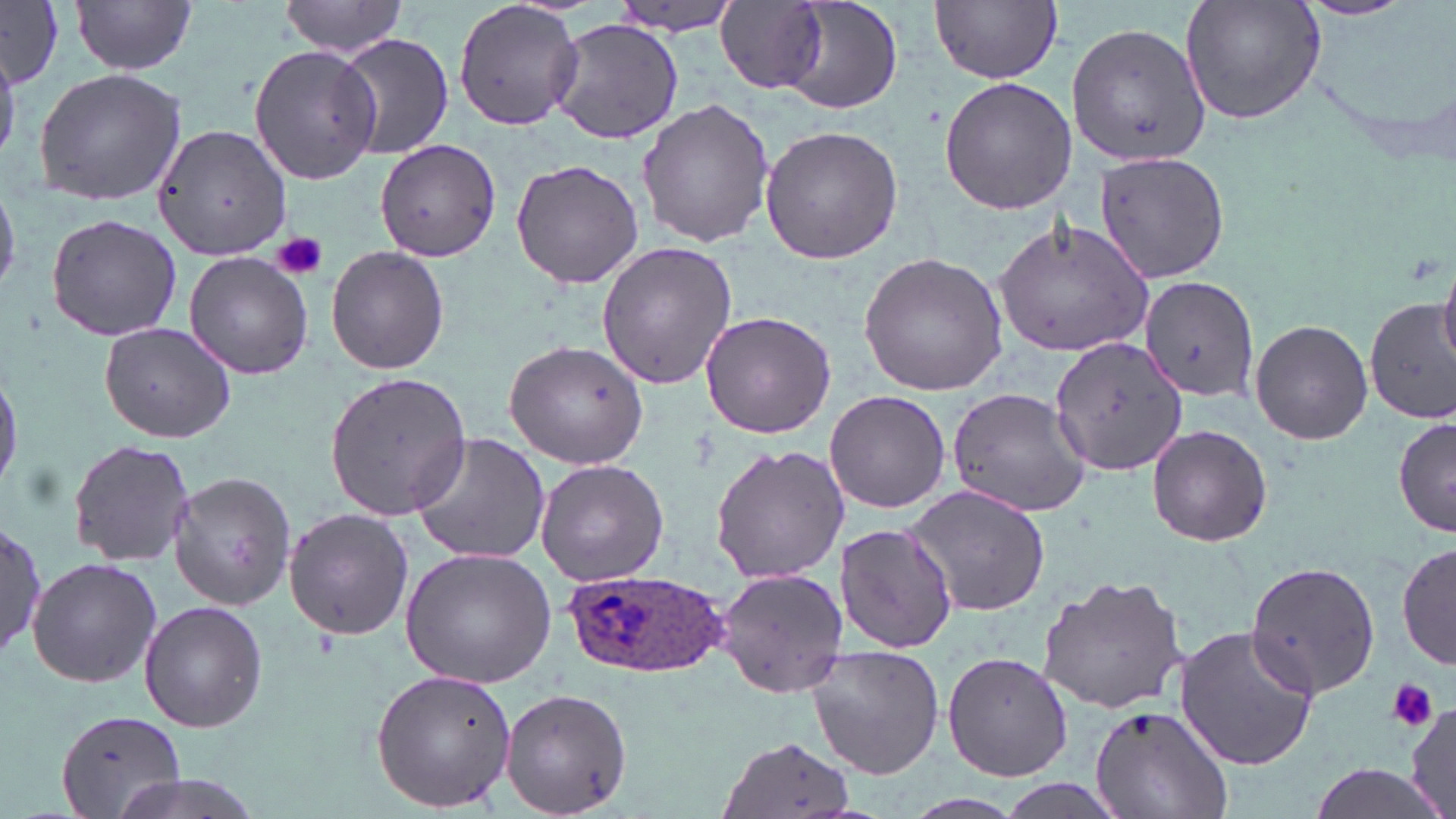

slide_level_diagnosis: Plasmodium ovale
field_of_view: single
image_size: 1456×819 pixels
plasmodium_ovale_infected_red_blood_cell_locations: 'approximate bounding boxes as (x1, y1, x2, y2) in pixels: (562, 569, 731, 677)'
platelet_locations: 'approximate bounding boxes as (x1, y1, x2, y2) in pixels: (274, 232, 328, 280), (1386, 678, 1439, 732)'
preparation: thin blood film
magnification: 1000x
modality: optical microscopy
stain: May-Grünwald-Giemsa
uninfected_red_blood_cell_locations: 'approximate bounding boxes as (x1, y1, x2, y2) in pixels: (72, 0, 197, 74), (774, 0, 902, 117), (931, 0, 1062, 84), (1180, 0, 1326, 126), (1293, 0, 1420, 21), (279, 1, 407, 57), (453, 1, 585, 135), (712, 1, 833, 95), (1, 2, 64, 85), (606, 2, 749, 37), (545, 20, 681, 144), (1066, 23, 1209, 165), (335, 31, 454, 162), (248, 44, 383, 183), (34, 66, 188, 207), (940, 75, 1076, 215), (637, 98, 774, 249), (155, 125, 292, 262), (758, 126, 902, 265), (374, 138, 500, 262), (1093, 153, 1231, 283), (509, 159, 643, 288), (45, 214, 184, 341), (992, 218, 1154, 359), (595, 240, 738, 390), (326, 245, 450, 375), (184, 251, 313, 379), (858, 251, 1008, 397), (1437, 262, 1456, 370), (1139, 274, 1259, 403), (1365, 295, 1456, 427), (699, 310, 837, 438), (1250, 319, 1374, 445), (100, 321, 238, 442), (1050, 335, 1187, 475), (504, 339, 648, 470), (0, 365, 22, 491), (324, 370, 474, 523), (946, 385, 1092, 517), (826, 391, 950, 512), (1395, 414, 1456, 535), (1146, 426, 1271, 546), (408, 431, 552, 567), (69, 436, 194, 569), (708, 445, 850, 584), (535, 459, 669, 587), (167, 472, 298, 610), (903, 483, 1052, 619), (283, 506, 414, 642), (0, 520, 48, 659), (840, 522, 954, 652), (1396, 537, 1454, 672), (400, 547, 557, 689), (26, 557, 163, 688), (1242, 559, 1384, 697), (714, 567, 848, 697), (1038, 575, 1190, 714), (141, 601, 266, 732), (1172, 624, 1321, 770), (805, 645, 946, 779), (940, 652, 1072, 784), (371, 669, 518, 812), (502, 688, 632, 817), (1405, 700, 1456, 814), (1089, 704, 1232, 819), (56, 707, 187, 819), (719, 735, 860, 819), (1304, 763, 1449, 819), (104, 774, 270, 819)'